Classify this cell by malaria status.
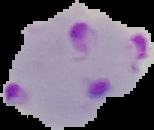

It is parasitized.

From a thin blood film. Image is 154×130 pixels. Cell region segmented out of the field of view; the surrounding area is masked to black.